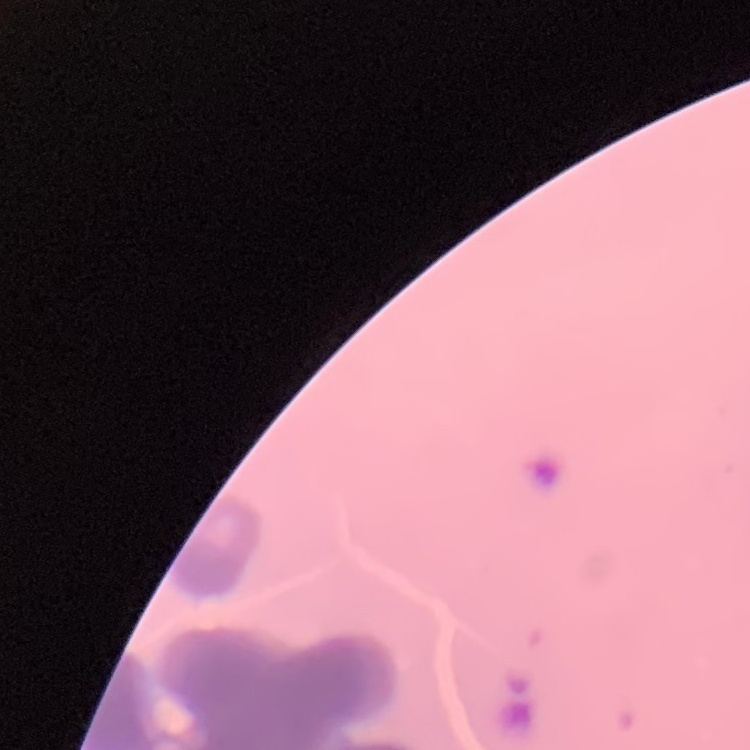
The erythrocytes show rouleaux formation. Stained with either Field's or Giemsa. Thin blood film. One tile cut from a larger photomicrograph.